State which parasite is depicted.
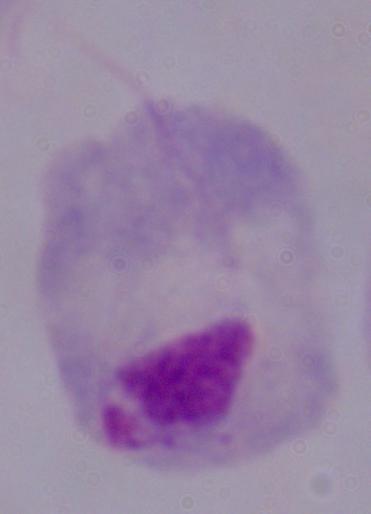
A trichomonad.

Summary:
  - Magnification: 1000x
  - Modality: photomicrograph